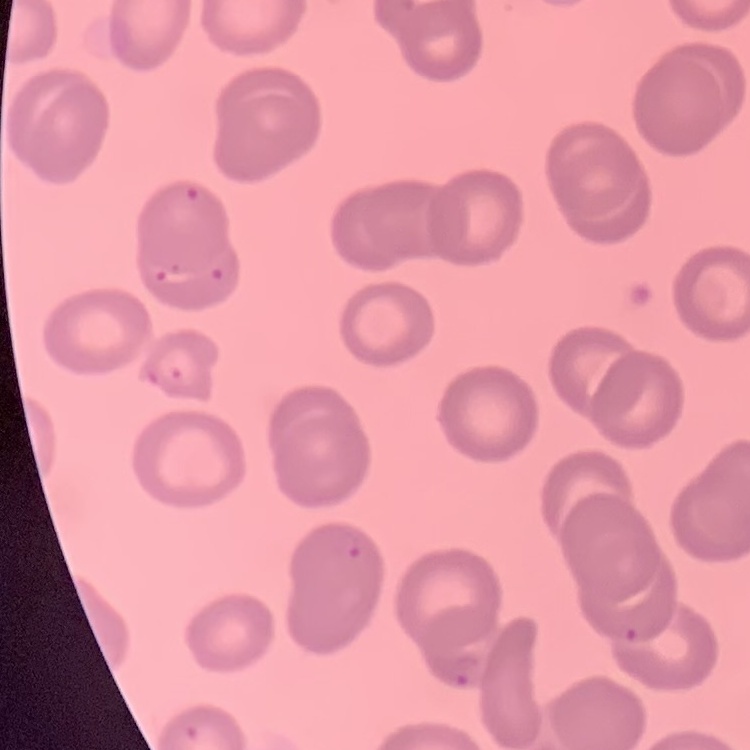
The red blood cells show no rouleaux formation. One tile cut from a larger photomicrograph. Field's or Giemsa stain. Thin blood smear.